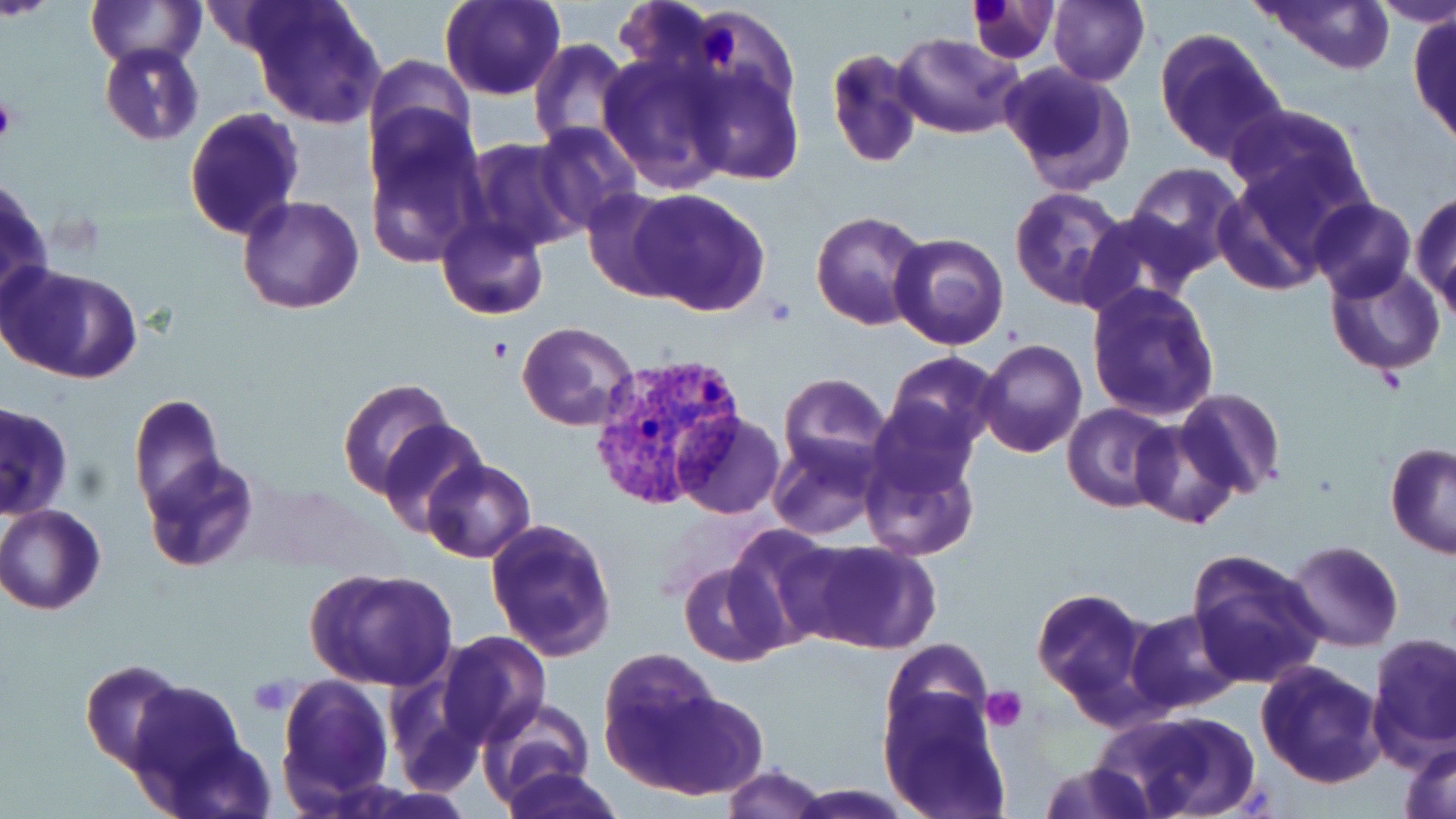

Approximate bounding boxes as named x1/y1/x2/y2 corners in pixels. Uninfected red blood cell locations: (x1=87, y1=0, x2=204, y2=67), (x1=440, y1=0, x2=566, y2=102), (x1=963, y1=0, x2=1059, y2=64), (x1=1047, y1=0, x2=1149, y2=85), (x1=1254, y1=0, x2=1398, y2=75), (x1=1370, y1=0, x2=1456, y2=28), (x1=245, y1=2, x2=384, y2=130), (x1=1408, y1=11, x2=1456, y2=150), (x1=1154, y1=29, x2=1288, y2=165), (x1=893, y1=32, x2=1024, y2=139), (x1=529, y1=39, x2=631, y2=150), (x1=99, y1=42, x2=203, y2=146), (x1=367, y1=47, x2=482, y2=159), (x1=824, y1=48, x2=924, y2=170), (x1=596, y1=52, x2=728, y2=193), (x1=684, y1=62, x2=805, y2=185), (x1=997, y1=63, x2=1135, y2=197), (x1=1225, y1=103, x2=1374, y2=221), (x1=183, y1=107, x2=304, y2=243), (x1=363, y1=113, x2=487, y2=266), (x1=535, y1=122, x2=642, y2=232), (x1=464, y1=139, x2=587, y2=255), (x1=1123, y1=163, x2=1243, y2=277), (x1=1215, y1=170, x2=1337, y2=295), (x1=0, y1=177, x2=51, y2=310), (x1=581, y1=186, x2=692, y2=301), (x1=1008, y1=186, x2=1131, y2=310), (x1=628, y1=187, x2=772, y2=316), (x1=1410, y1=189, x2=1456, y2=312), (x1=236, y1=195, x2=364, y2=314), (x1=1309, y1=197, x2=1415, y2=301), (x1=810, y1=210, x2=930, y2=330), (x1=1080, y1=210, x2=1203, y2=316), (x1=437, y1=217, x2=549, y2=320), (x1=890, y1=232, x2=1009, y2=351), (x1=1326, y1=262, x2=1446, y2=379), (x1=1, y1=264, x2=144, y2=385), (x1=1086, y1=281, x2=1221, y2=421), (x1=517, y1=322, x2=639, y2=432), (x1=975, y1=339, x2=1086, y2=458), (x1=882, y1=351, x2=1002, y2=457), (x1=778, y1=373, x2=891, y2=477), (x1=337, y1=377, x2=455, y2=500), (x1=1174, y1=386, x2=1287, y2=499), (x1=870, y1=392, x2=982, y2=499), (x1=128, y1=393, x2=226, y2=516), (x1=0, y1=400, x2=73, y2=520), (x1=1062, y1=403, x2=1178, y2=512), (x1=672, y1=412, x2=785, y2=519), (x1=378, y1=419, x2=486, y2=536), (x1=1130, y1=420, x2=1243, y2=530), (x1=768, y1=436, x2=883, y2=541), (x1=859, y1=443, x2=980, y2=561), (x1=1384, y1=443, x2=1456, y2=560), (x1=141, y1=453, x2=258, y2=574), (x1=421, y1=459, x2=536, y2=564), (x1=0, y1=504, x2=106, y2=615), (x1=483, y1=515, x2=619, y2=662), (x1=720, y1=526, x2=835, y2=650), (x1=791, y1=537, x2=939, y2=655), (x1=1279, y1=540, x2=1404, y2=652), (x1=1186, y1=548, x2=1329, y2=689), (x1=678, y1=563, x2=787, y2=665), (x1=305, y1=567, x2=459, y2=691), (x1=1032, y1=586, x2=1151, y2=711), (x1=1127, y1=607, x2=1244, y2=714), (x1=437, y1=632, x2=551, y2=748), (x1=1366, y1=634, x2=1456, y2=764), (x1=879, y1=637, x2=995, y2=748), (x1=597, y1=645, x2=724, y2=767), (x1=80, y1=658, x2=190, y2=773), (x1=1254, y1=660, x2=1385, y2=789), (x1=275, y1=674, x2=394, y2=808), (x1=633, y1=689, x2=768, y2=800), (x1=879, y1=690, x2=1011, y2=819), (x1=130, y1=692, x2=262, y2=811), (x1=477, y1=697, x2=597, y2=806), (x1=1097, y1=710, x2=1255, y2=819), (x1=1401, y1=740, x2=1456, y2=819), (x1=1038, y1=761, x2=1159, y2=819), (x1=722, y1=765, x2=831, y2=819), (x1=501, y1=766, x2=624, y2=819), (x1=789, y1=784, x2=913, y2=816). Plasmodium vivax-infected red blood cell locations: (x1=585, y1=352, x2=747, y2=513). Platelet locations: (x1=701, y1=24, x2=741, y2=60), (x1=0, y1=93, x2=17, y2=146), (x1=979, y1=687, x2=1026, y2=733). Slide-level diagnosis: Plasmodium vivax. May-Grünwald-Giemsa stain. Thin blood smear. Captured at 1000x magnification. Image is 1456×819 pixels. Optical microscopy. Single field of view.